Locate every Plasmodium parasite by life-cycle stage, and every leukocyte.
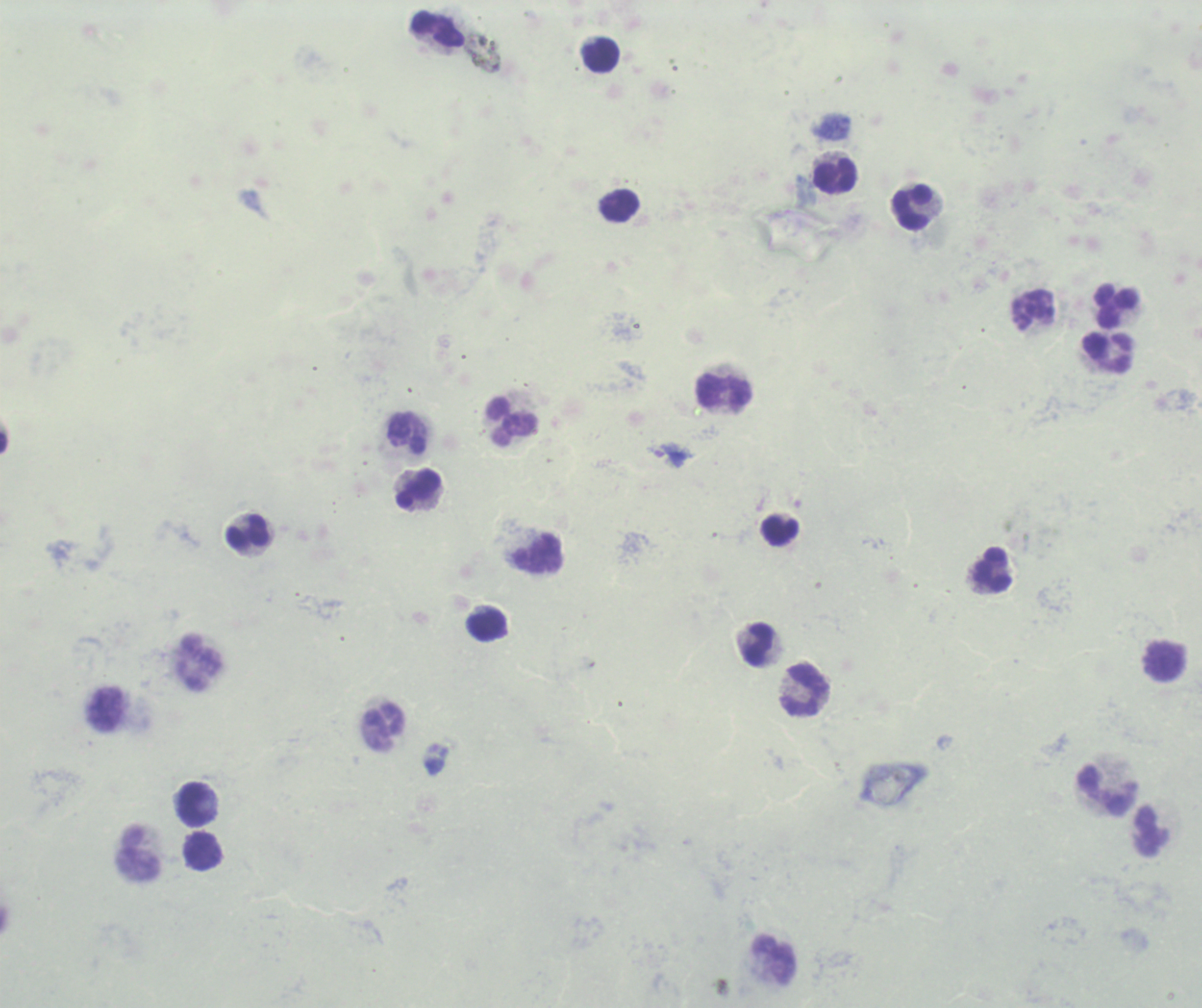
Approximate centers as [x, y] in pixels.
Trophozoites: [672, 455].
No schizont or gametocyte forms observed.
Leukocytes: [437, 30], [601, 55], [835, 177], [620, 206], [911, 207], [1115, 307], [1032, 309], [1108, 353], [724, 393], [511, 422], [407, 433], [417, 489], [779, 532], [248, 533], [537, 554], [991, 569], [487, 627], [759, 645], [1164, 661], [199, 662], [805, 691], [106, 709], [383, 727], [1107, 792], [196, 804], [1151, 832], [204, 852], [139, 855], [773, 961].

Summary:
  - Image size: 1202×1008 pixels
  - Context: previously used in a real diagnosis
  - Stain: Romanowsky
  - Preparation: thick blood film
  - Magnification: 100x
  - Background quality: unsatisfactory
  - Field of view: single